Give the position of every leukocyte visible.
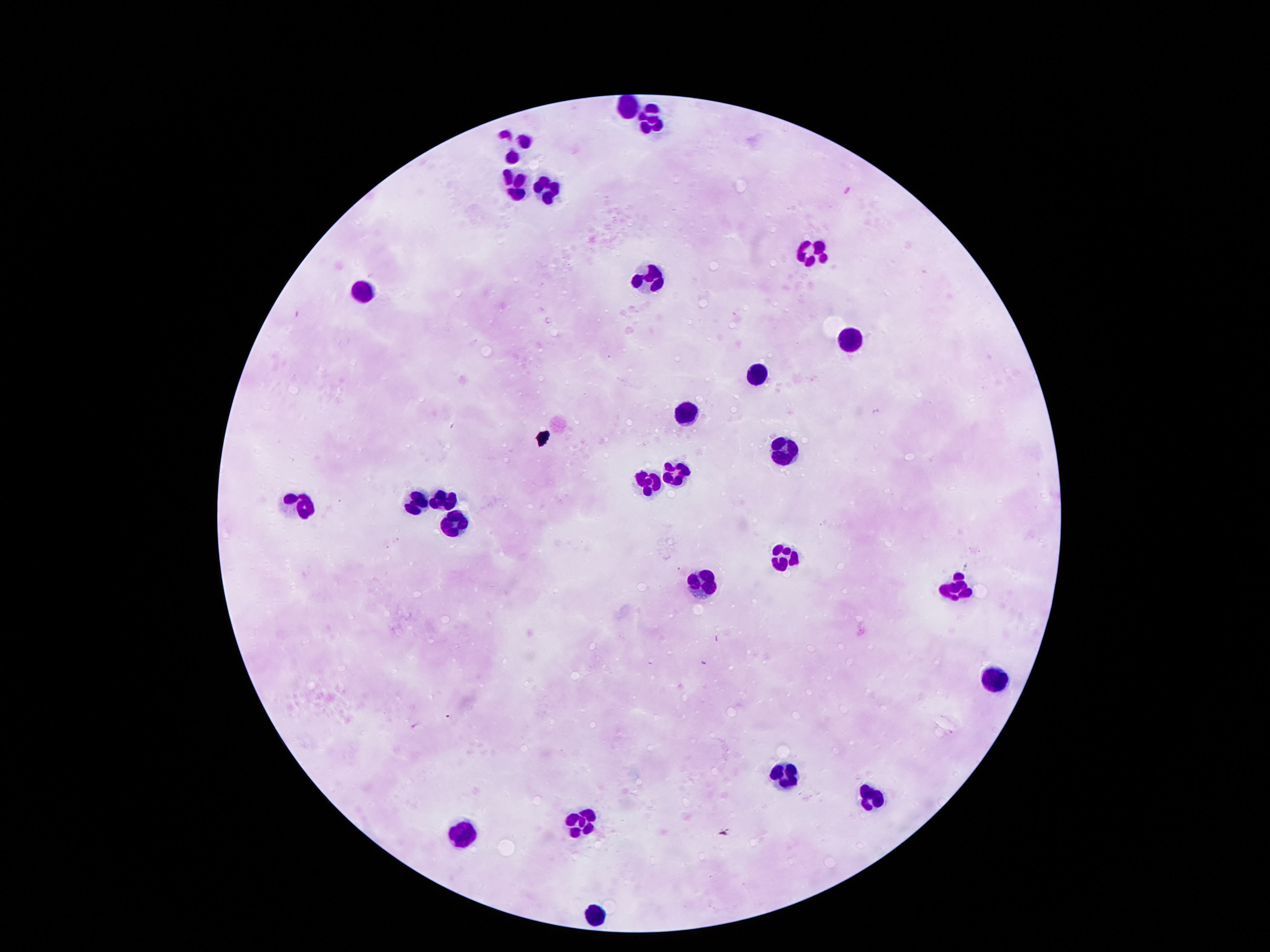

Approximate centers as (x, y) in pixels.
Leukocytes: (626, 104), (647, 125), (514, 139), (511, 182), (549, 189), (810, 251), (649, 284), (357, 289), (849, 336), (760, 375), (688, 408), (779, 445), (674, 469), (649, 478), (444, 501), (418, 503), (301, 504), (451, 524), (779, 557), (696, 583), (953, 591), (999, 676), (778, 775), (869, 797), (583, 819), (461, 835), (591, 909).

patient malaria status = uninfected
magnification = 100x
capture = smartphone camera through the microscope eyepiece
stain = Giemsa
image size = 1270×952 pixels
preparation = thick peripheral-blood smear
field of view = single